State which parasite is depicted.
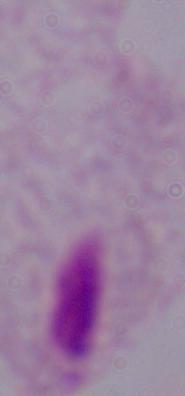
A trichomonad.

Captured at 1000x magnification. Photomicrograph.